Outline each Plasmodium vivax-infected red blood cell.
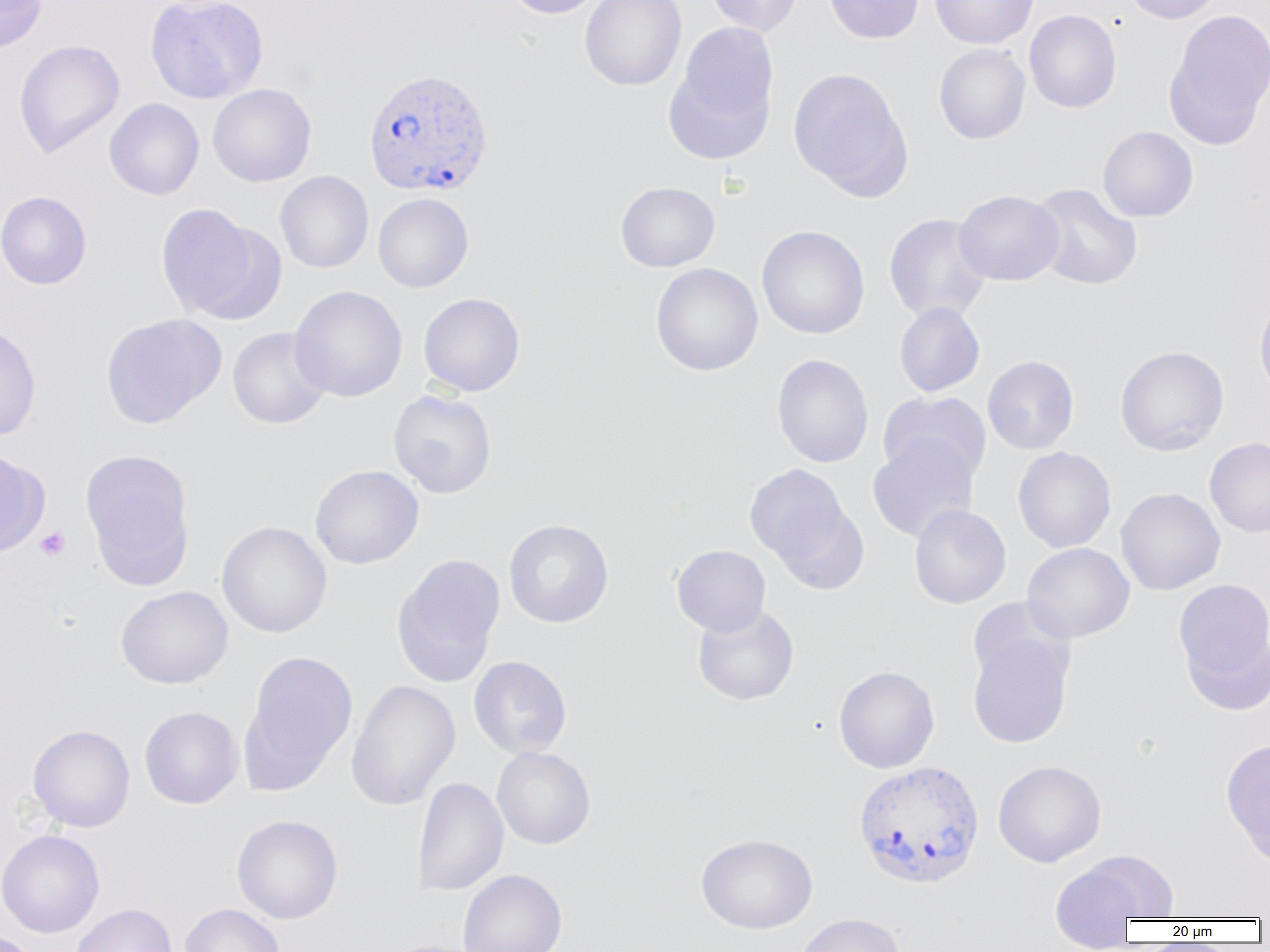

Approximate bounding boxes as (x1, y1, x2, y2) in pixels.
Plasmodium vivax-infected red blood cells: (363, 67, 494, 197), (853, 760, 985, 888).

slide-level diagnosis = Plasmodium vivax
field of view = single
magnification = 1000x
platelet locations = approximate bounding boxes as (x1, y1, x2, y2) in pixels: (35, 527, 71, 562)
preparation = thin blood smear
uninfected red blood cell locations = approximate bounding boxes as (x1, y1, x2, y2) in pixels: (0, 0, 47, 53), (144, 0, 269, 104), (504, 0, 606, 19), (580, 0, 686, 91), (705, 0, 805, 36), (824, 0, 923, 43), (930, 0, 1038, 49), (1120, 0, 1225, 24), (1166, 9, 1270, 143), (1024, 10, 1122, 113), (666, 24, 779, 161), (13, 39, 125, 159), (933, 43, 1030, 144), (787, 67, 912, 199), (207, 83, 316, 187), (104, 98, 204, 200), (1098, 126, 1198, 222), (275, 170, 373, 273), (616, 182, 719, 272), (1029, 183, 1143, 290), (954, 190, 1064, 285), (0, 191, 92, 289), (373, 193, 474, 292), (155, 203, 280, 324), (884, 213, 992, 324), (757, 225, 869, 339), (651, 262, 763, 375), (289, 285, 407, 402), (418, 293, 525, 396), (1254, 294, 1270, 403), (894, 302, 985, 397), (99, 313, 225, 429), (0, 323, 42, 441), (227, 327, 331, 429), (1115, 345, 1229, 456), (772, 354, 874, 468), (982, 355, 1079, 454), (388, 389, 496, 498), (878, 391, 991, 485), (867, 436, 980, 543), (1205, 437, 1270, 537), (1013, 446, 1116, 553), (0, 448, 48, 557), (80, 448, 196, 589), (744, 463, 857, 577), (310, 464, 424, 569), (1115, 487, 1226, 595), (909, 504, 1011, 608), (503, 519, 613, 627), (216, 521, 332, 638), (1022, 542, 1135, 643), (672, 545, 770, 636), (392, 554, 505, 688), (1172, 579, 1270, 690), (116, 585, 233, 689), (693, 604, 799, 705), (1180, 624, 1270, 716), (968, 632, 1073, 748), (242, 650, 358, 787), (469, 656, 571, 758), (834, 665, 939, 773), (346, 679, 460, 811), (139, 706, 243, 809), (27, 724, 135, 832), (1220, 736, 1270, 867), (492, 746, 595, 849), (993, 760, 1106, 867), (410, 777, 508, 896), (231, 814, 343, 924), (0, 829, 104, 938), (696, 833, 817, 934), (1070, 850, 1179, 922), (1049, 860, 1149, 949), (457, 869, 567, 952), (69, 903, 178, 952), (180, 904, 285, 952), (796, 913, 905, 952), (0, 931, 40, 952), (379, 939, 489, 952)
modality = optical microscopy
image size = 1270×952 pixels